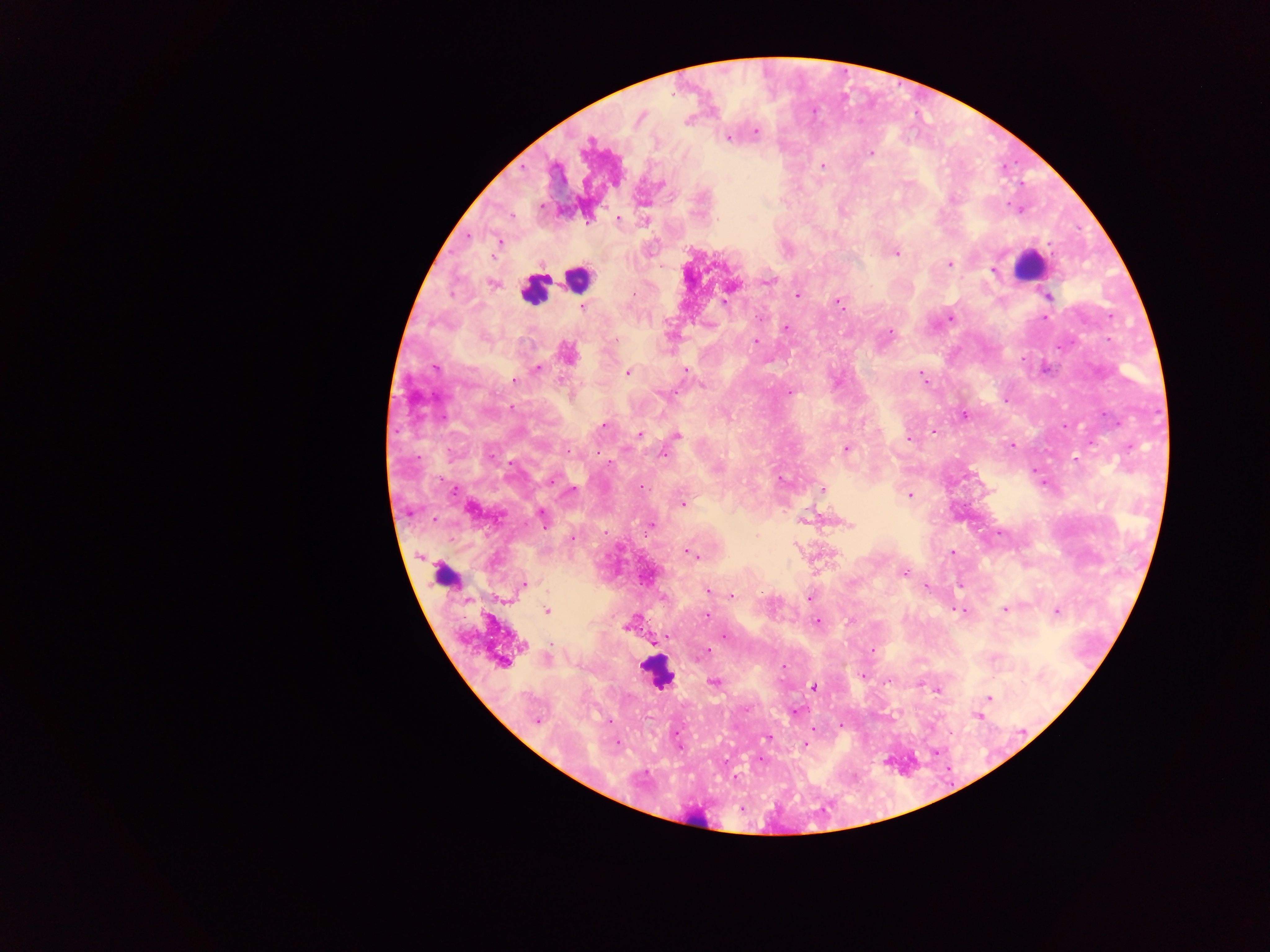

capture = mobile-phone photograph through a microscope
country = Ghana
image size = 1270×952 pixels
field of view = single
leukocyte locations = approximate centers as [x, y] in pixels: [1028, 266], [576, 279], [533, 290], [445, 577], [655, 673], [698, 822]
Plasmodium parasite locations = approximate centers as [x, y] in pixels: [640, 118], [756, 132], [728, 138], [870, 153], [824, 165], [661, 184], [617, 218], [500, 242], [895, 253], [949, 264], [993, 270], [768, 282], [492, 284], [634, 294], [796, 294], [1047, 296], [725, 301], [838, 302], [583, 308], [760, 318], [951, 318], [1045, 318], [786, 328], [891, 332], [671, 336], [756, 342], [568, 354], [435, 368], [538, 369], [686, 370], [627, 373], [922, 376], [515, 380], [702, 385], [790, 393], [1005, 401], [964, 415], [604, 426], [932, 430], [639, 434], [677, 435], [908, 439], [1012, 445], [846, 448], [569, 451], [665, 454], [1075, 459], [552, 479], [780, 480], [823, 489], [572, 490], [453, 491], [910, 496], [683, 504], [542, 517], [803, 520], [849, 524], [651, 526], [1000, 533], [572, 538], [688, 552], [952, 552], [692, 555], [904, 573], [524, 585], [926, 586], [708, 591], [732, 595], [809, 598], [960, 610], [1005, 610], [547, 611], [1056, 611], [707, 616], [848, 621], [817, 622], [725, 636], [668, 637], [654, 642], [524, 646], [871, 651], [703, 654], [502, 663], [783, 667], [863, 677], [886, 682], [714, 683], [814, 686], [936, 690], [990, 698], [796, 712], [977, 716], [537, 721], [608, 721], [766, 738], [617, 743], [805, 744], [680, 746]
preparation = thick blood film